Report the malaria status of this cell.
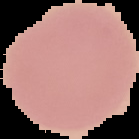
Uninfected.

image size = 139×139 pixels
preparation = thin blood film
image type = segmented cell region on a black background